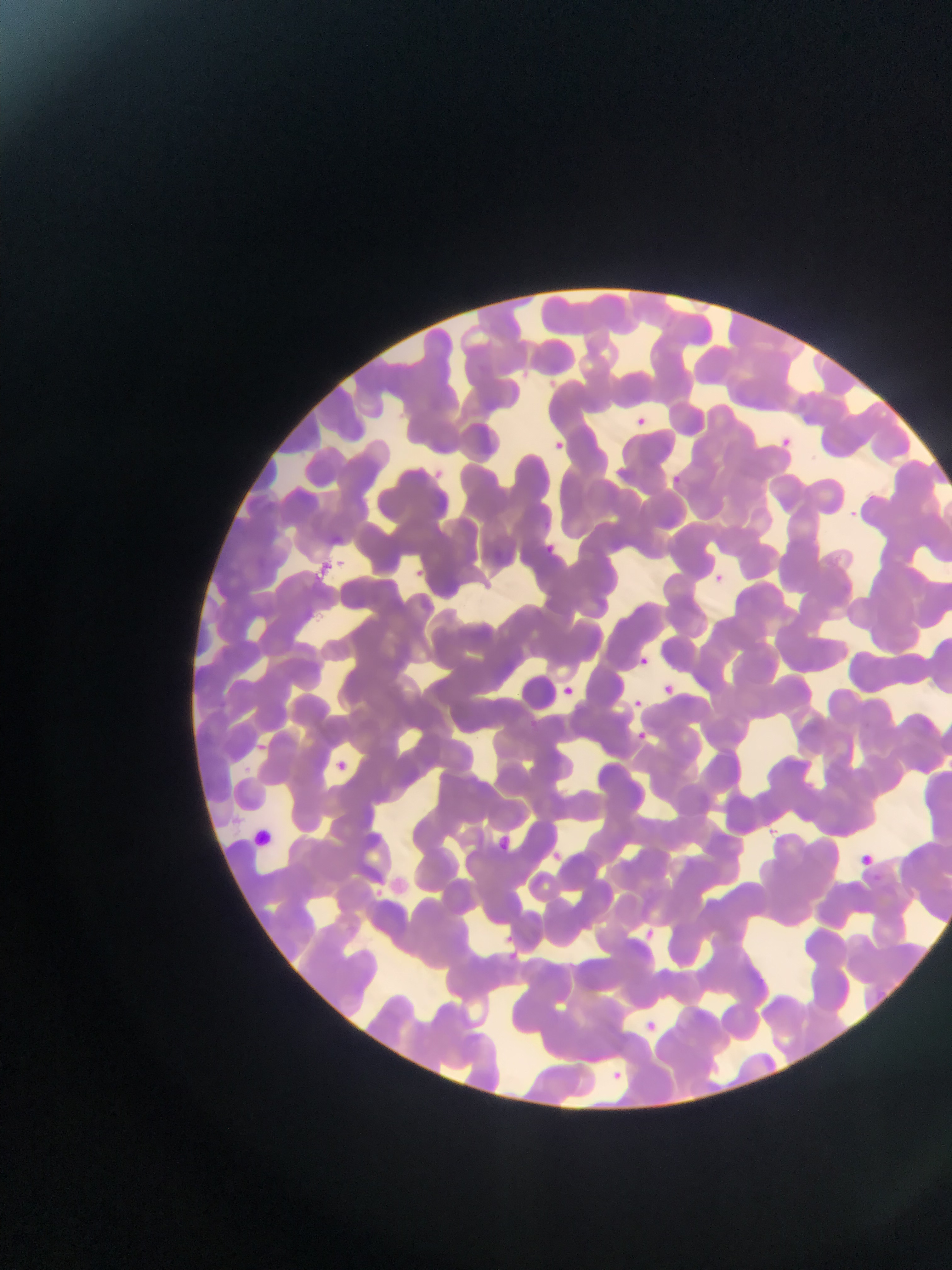

{
  "capture": "mobile-phone photograph through a microscope",
  "preparation": "thin blood film",
  "country": "Ghana",
  "leukocyte_locations": "approximate bounding boxes as {left, top, right, bottom} in pixels: {248, 824, 278, 854}",
  "malaria_parasite_locations": "approximate bounding boxes as {left, top, right, bottom} in pixels: {516, 367, 533, 382}, {631, 415, 648, 430}, {774, 434, 795, 456}, {546, 437, 566, 455}, {428, 462, 448, 478}, {670, 471, 683, 488}, {842, 500, 863, 526}, {541, 535, 564, 556}, {312, 557, 339, 579}, {409, 565, 432, 578}, {710, 570, 737, 590}, {634, 649, 648, 669}, {662, 680, 672, 691}, {560, 682, 578, 692}, {630, 693, 642, 704}, {631, 724, 652, 738}, {332, 749, 352, 766}, {488, 829, 517, 851}, {547, 847, 575, 869}, {860, 851, 879, 868}, {373, 885, 395, 903}, {645, 926, 664, 943}, {499, 928, 513, 941}, {504, 947, 521, 963}, {637, 1016, 663, 1040}, {608, 1063, 622, 1071}",
  "field_of_view": "single",
  "image_size": "952×1270 pixels"
}